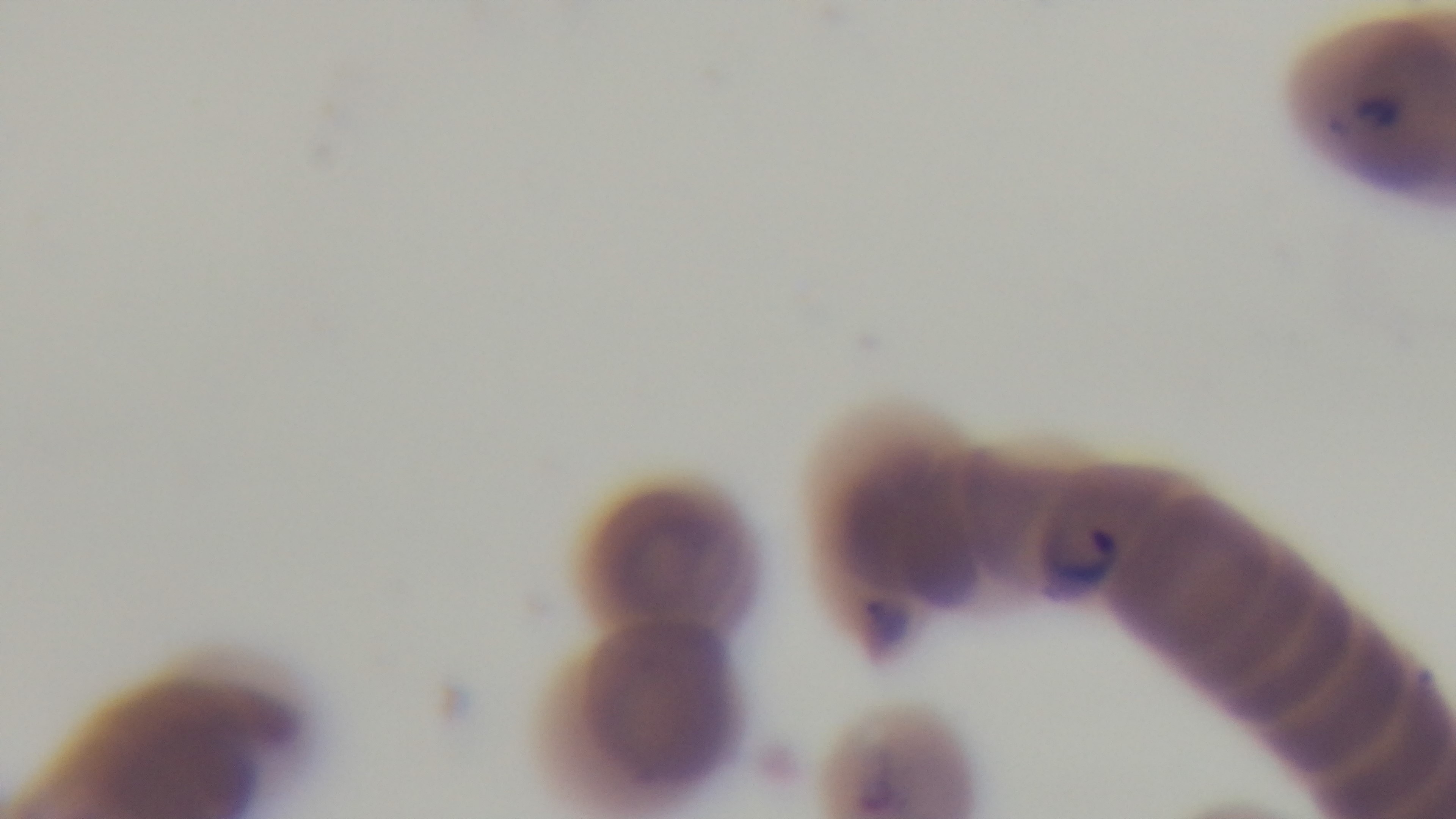

{
  "modality": "light microscopy",
  "objective": "100x oil immersion",
  "field_of_view": "single",
  "malaria_status": "positive",
  "capture": "mounted 4K digital camera",
  "stain": "Giemsa",
  "preparation": "thin"
}